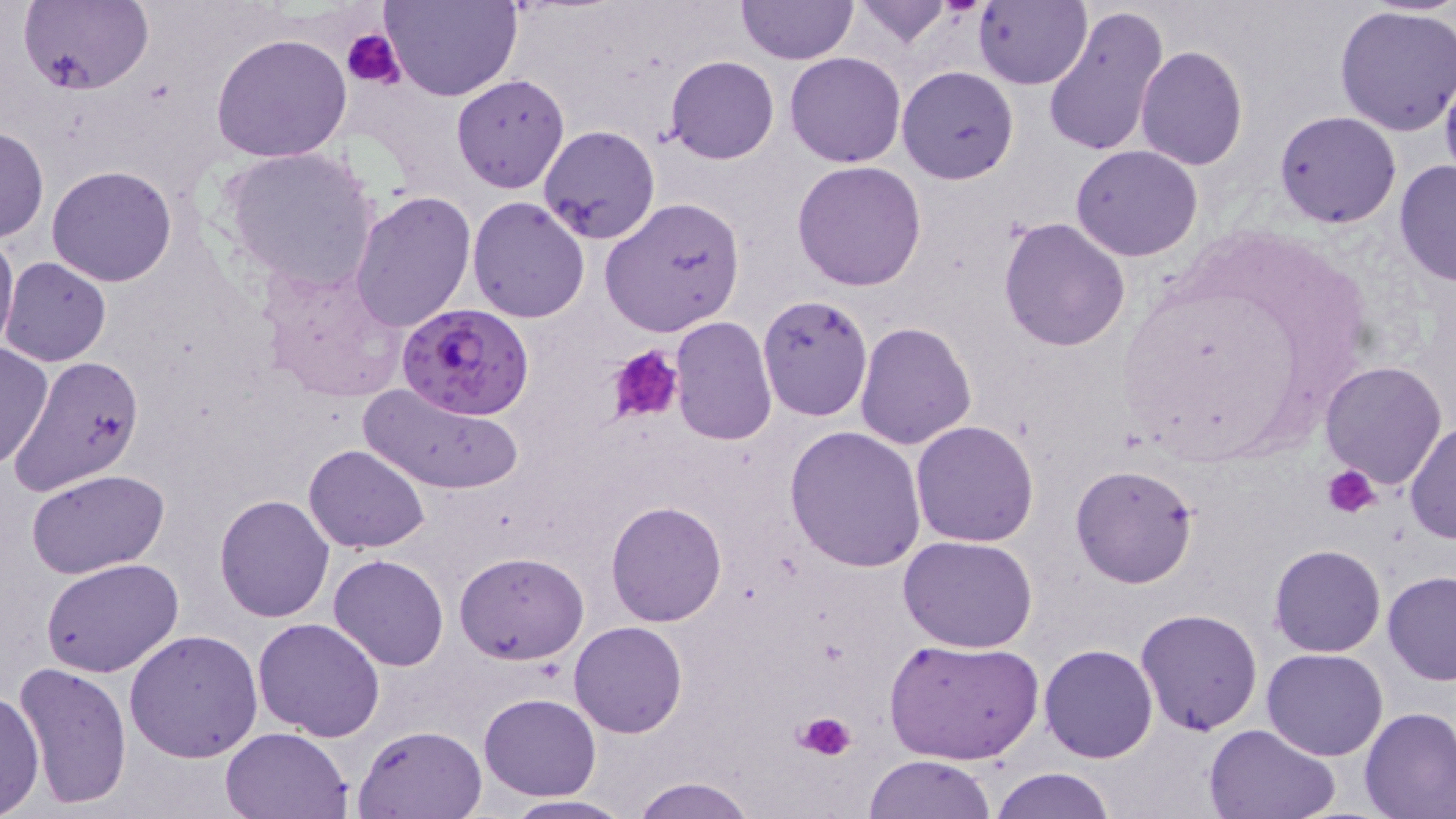

Approximate bounding boxes as [x1, y1, x2, y2] in pixels. Plasmodium falciparum-infected red blood cell locations: [397, 302, 534, 420]. Platelet locations: [342, 29, 406, 89], [608, 345, 686, 426], [1321, 461, 1382, 519], [794, 708, 856, 762]. Uninfected red blood cell locations: [19, 0, 153, 96], [383, 0, 521, 103], [852, 0, 958, 49], [972, 0, 1092, 90], [735, 1, 858, 66], [1044, 3, 1169, 160], [1333, 5, 1456, 138], [209, 30, 353, 162], [1135, 46, 1248, 171], [785, 51, 907, 167], [666, 56, 779, 165], [896, 66, 1020, 184], [1439, 70, 1456, 190], [451, 73, 570, 193], [1274, 110, 1402, 228], [1, 124, 48, 244], [538, 125, 659, 245], [219, 144, 381, 294], [1070, 145, 1203, 261], [791, 159, 927, 290], [1393, 159, 1455, 288], [45, 165, 178, 286], [348, 189, 477, 333], [466, 195, 592, 322], [599, 197, 746, 338], [999, 218, 1131, 355], [0, 223, 18, 358], [3, 257, 111, 367], [259, 259, 407, 405], [757, 294, 873, 422], [669, 315, 777, 446], [855, 321, 977, 450], [0, 342, 53, 471], [7, 352, 147, 494], [1320, 361, 1447, 487], [360, 381, 525, 495], [1405, 418, 1456, 546], [911, 420, 1039, 546], [785, 426, 926, 573], [303, 443, 430, 553], [1070, 464, 1201, 587], [26, 469, 171, 579], [215, 494, 335, 621], [606, 500, 727, 626], [897, 535, 1040, 653], [1269, 544, 1386, 658], [454, 551, 587, 663], [328, 554, 449, 671], [40, 558, 185, 679], [1384, 571, 1456, 684], [1134, 608, 1263, 736], [251, 616, 385, 740], [569, 620, 687, 737], [124, 629, 263, 762], [884, 637, 1043, 765], [1040, 644, 1158, 763], [1262, 647, 1389, 761], [13, 660, 134, 807], [0, 687, 44, 816], [478, 693, 601, 801], [1359, 706, 1456, 819], [1203, 722, 1340, 819], [353, 725, 486, 818], [220, 726, 353, 818], [865, 753, 998, 819], [993, 767, 1115, 819], [629, 776, 758, 819], [501, 793, 637, 818]. Slide-level diagnosis: Plasmodium falciparum. Light microscopy. Single field of view. Thin blood film. May-Grünwald-Giemsa stain. Image is 1456×819 pixels. Captured at 1000x magnification.